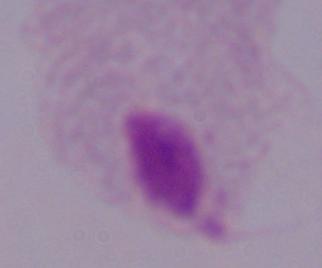

identification = trichomonad
modality = photomicrograph
magnification = 1000x